Classify this cell by malaria status.
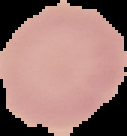
Uninfected.

Summary:
  - Image size: 127×136 pixels
  - Image type: cell region segmented out of the field of view; surrounding area masked to black
  - Preparation: thin blood film